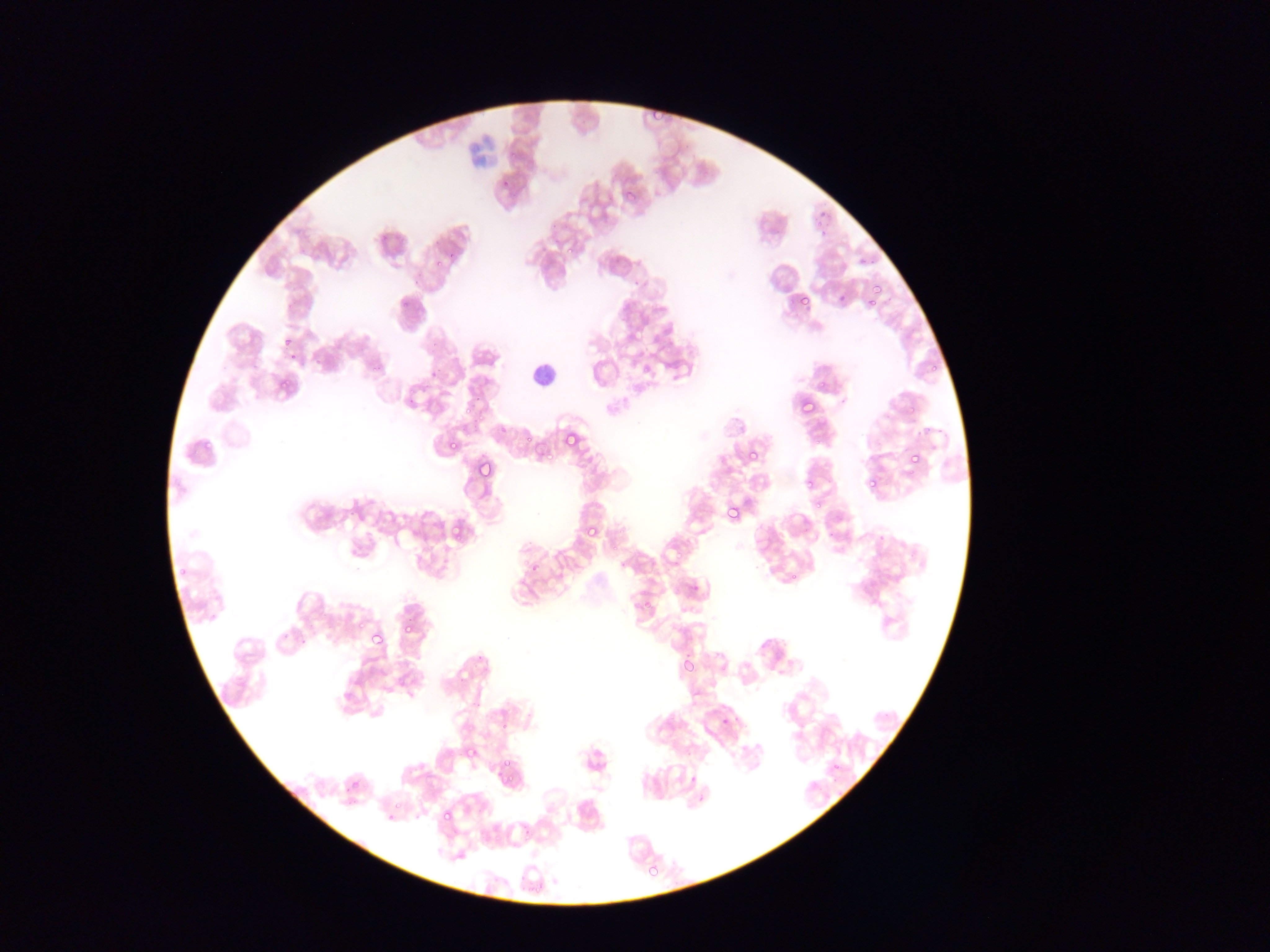

preparation = thin blood smear
capture = mobile-phone photograph through a microscope
leukocyte locations = approximate bounding boxes as [left, top, right, bottom] in pixels: [528, 355, 560, 396]
field of view = single
country = Ghana
Plasmodium parasite locations = approximate bounding boxes as [left, top, right, bottom] in pixels: [815, 209, 832, 230], [554, 231, 577, 253], [856, 254, 874, 270], [870, 278, 886, 295], [796, 293, 812, 311], [859, 295, 881, 309], [283, 333, 303, 354], [281, 335, 295, 351], [273, 374, 293, 395], [792, 395, 818, 421], [925, 426, 948, 449], [448, 432, 462, 452], [562, 434, 578, 456], [202, 437, 214, 450], [747, 448, 764, 466], [905, 449, 924, 470], [476, 457, 497, 480], [862, 464, 879, 495], [804, 482, 813, 494], [811, 499, 826, 515], [724, 501, 745, 523], [443, 520, 466, 544], [584, 524, 602, 543], [527, 561, 541, 577], [400, 622, 415, 638], [370, 630, 385, 648], [680, 655, 696, 673], [343, 675, 363, 700], [719, 715, 733, 730], [461, 742, 480, 762], [497, 755, 516, 775], [346, 775, 364, 794], [439, 806, 457, 826], [645, 861, 662, 880]
image size = 1270×952 pixels